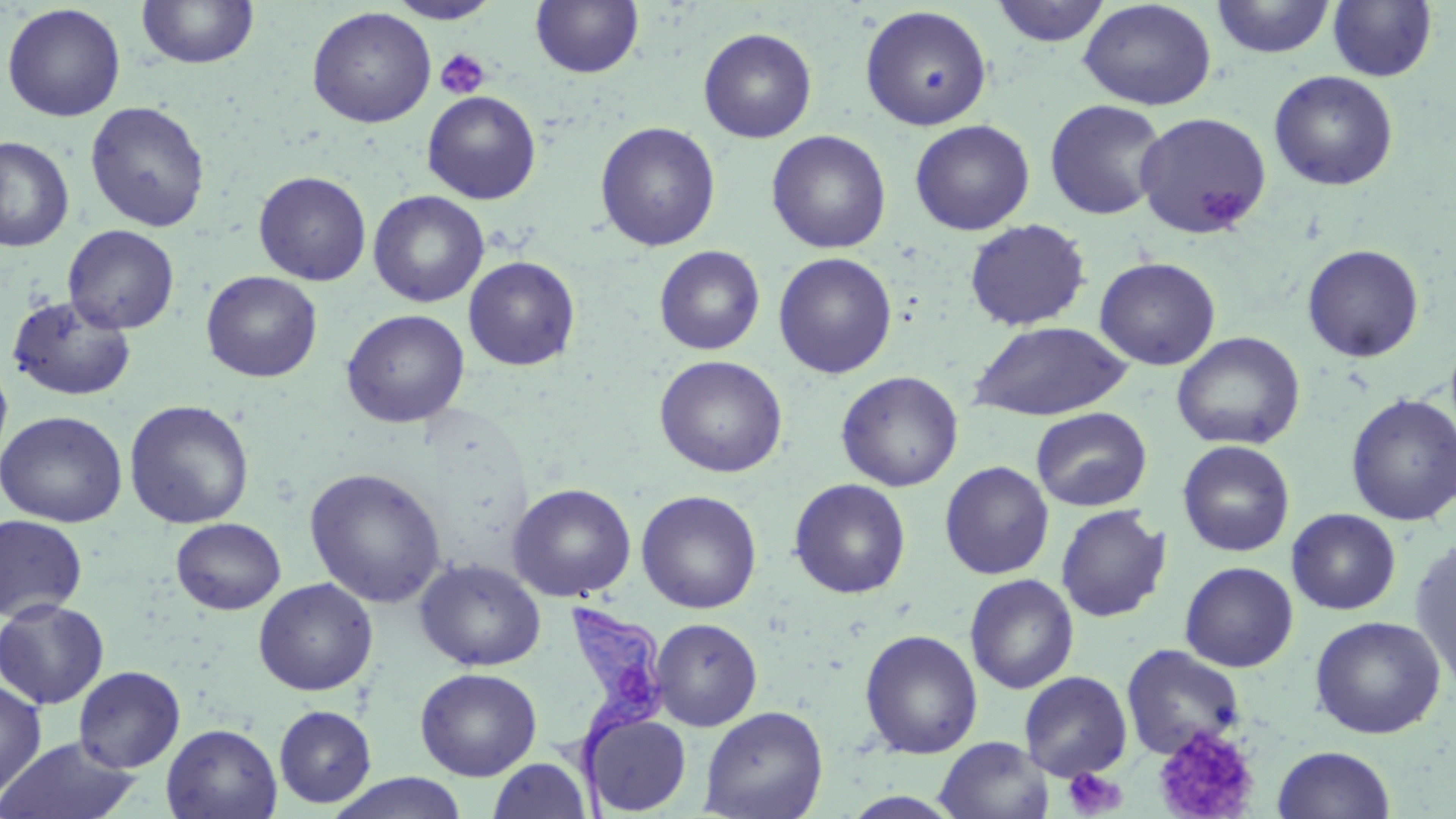

Approximate bounding boxes as (x1,y1)-(x2,y2) corner pairs in pixels. Uninfected red blood cell locations: (135,0)-(260,70), (991,0)-(1112,47), (1211,0)-(1335,59), (385,1)-(501,24), (530,1)-(644,78), (1077,1)-(1216,110), (1327,1)-(1437,82), (1,3)-(126,122), (859,5)-(993,131), (306,6)-(437,128), (698,27)-(817,143), (1268,70)-(1398,191), (422,90)-(541,204), (1044,98)-(1169,220), (85,101)-(210,232), (1133,112)-(1272,238), (909,119)-(1035,235), (595,121)-(721,252), (766,130)-(891,254), (1,136)-(74,252), (253,171)-(371,285), (368,190)-(489,307), (963,218)-(1091,332), (63,224)-(179,334), (1302,243)-(1425,362), (654,245)-(765,355), (773,252)-(897,378), (463,256)-(580,371), (1095,257)-(1221,370), (200,270)-(323,382), (7,295)-(137,402), (341,309)-(470,428), (967,321)-(1134,421), (1171,331)-(1305,451), (0,355)-(13,466), (654,355)-(788,478), (836,370)-(963,492), (1345,394)-(1456,526), (124,399)-(254,529), (1030,407)-(1152,512), (0,411)-(127,527), (1177,440)-(1295,556), (939,461)-(1054,579), (305,467)-(446,608), (788,478)-(911,598), (507,482)-(637,602), (636,490)-(762,614), (1055,505)-(1171,623), (1286,508)-(1400,615), (0,514)-(87,622), (170,518)-(287,614), (1409,538)-(1456,693), (415,558)-(546,671), (1179,561)-(1299,672), (964,574)-(1079,694), (253,578)-(377,696), (0,598)-(109,709), (1309,615)-(1446,739), (650,617)-(763,730), (859,629)-(983,759), (1121,643)-(1246,759), (73,665)-(186,772), (414,667)-(542,781), (1019,670)-(1133,781), (0,679)-(47,800), (273,705)-(376,808), (699,706)-(828,819), (583,713)-(692,815), (161,723)-(283,818), (0,736)-(143,819), (934,736)-(1053,819), (1272,745)-(1396,819), (488,757)-(592,819), (327,773)-(469,819). Platelet locations: (434,48)-(490,100), (1195,186)-(1246,226), (1154,725)-(1260,819), (1062,766)-(1127,817). Trypanosoma brucei locations: (548,603)-(666,818). Slide-level diagnosis: Trypanosoma brucei. One field of a larger specimen. 1000x magnification. Thin blood smear. Light microscopy. May-Grünwald-Giemsa-stained preparation. Image is 1456×819 pixels.